State the blood parasite species.
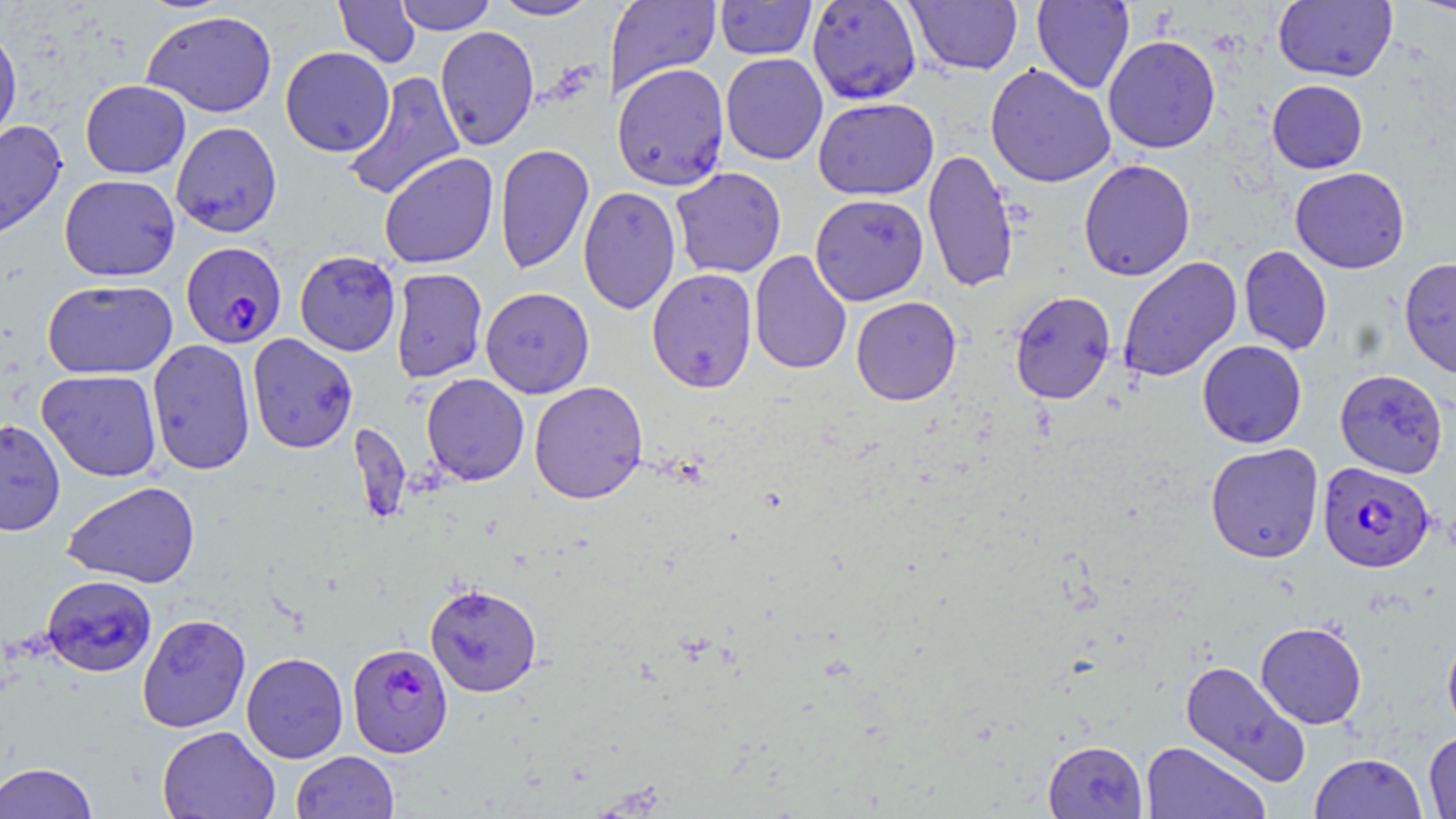

Plasmodium falciparum.

Approximate bounding boxes as (x1, y1, x2, y2) in pixels. Plasmodium falciparum-infected red blood cell locations: (181, 241, 287, 348), (1317, 462, 1434, 572), (346, 642, 453, 757). Uninfected red blood cell locations: (333, 0, 421, 68), (395, 0, 496, 35), (491, 0, 602, 21), (605, 0, 722, 96), (806, 0, 922, 105), (905, 0, 1023, 75), (1273, 0, 1398, 82), (1403, 0, 1456, 19), (714, 1, 817, 60), (1032, 1, 1134, 93), (143, 10, 277, 118), (434, 25, 539, 151), (0, 26, 23, 152), (1103, 35, 1221, 153), (280, 47, 395, 157), (720, 53, 828, 165), (611, 62, 730, 191), (985, 63, 1116, 188), (343, 71, 466, 202), (1267, 79, 1368, 173), (80, 80, 191, 178), (813, 97, 939, 200), (0, 119, 68, 243), (170, 121, 283, 237), (495, 143, 595, 274), (923, 149, 1019, 293), (378, 152, 499, 269), (1078, 159, 1196, 281), (670, 166, 786, 278), (1290, 167, 1410, 273), (59, 174, 180, 281), (578, 186, 681, 314), (810, 194, 929, 306), (1238, 246, 1332, 355), (294, 250, 401, 356), (750, 250, 852, 374), (1117, 256, 1242, 383), (1399, 257, 1456, 379), (390, 268, 488, 382), (647, 268, 757, 392), (42, 279, 178, 380), (480, 287, 594, 399), (1009, 290, 1116, 404), (851, 296, 962, 405), (247, 334, 358, 454), (147, 339, 255, 476), (1197, 340, 1307, 449), (37, 369, 162, 481), (1334, 369, 1449, 479), (421, 373, 530, 485), (529, 381, 648, 504), (0, 418, 66, 536), (1205, 443, 1324, 563), (62, 481, 200, 588), (41, 575, 157, 677), (424, 582, 543, 698), (137, 613, 251, 733), (1255, 622, 1367, 729), (1442, 630, 1456, 739), (241, 652, 349, 763), (1179, 659, 1311, 786), (157, 726, 281, 819), (1423, 731, 1456, 819), (1043, 740, 1148, 818), (1140, 741, 1270, 819), (290, 751, 399, 819), (1309, 752, 1428, 819), (0, 761, 99, 819). 1000x magnification. May-Grünwald-Giemsa-stained preparation. Light microscopy. Thin blood smear. Image is 1456×819 pixels. Single field of view.